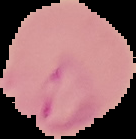

Summary:
  - Preparation: thin blood smear
  - Image size: 136×139 pixels
  - Malaria status: parasitized
  - Image type: segmented cell region with the area outside set to black